Locate every uninfected red blood cell.
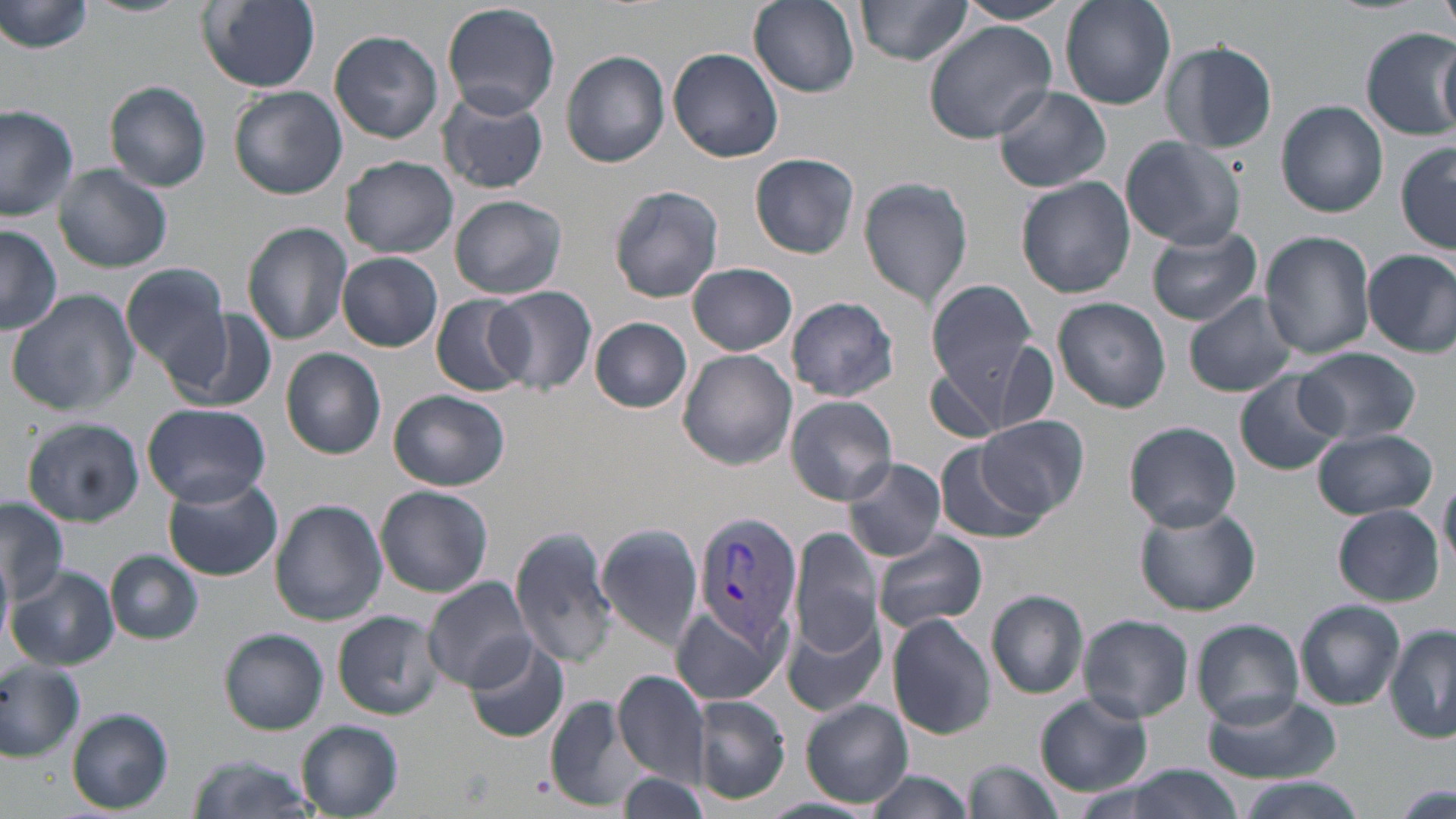
Approximate bounding boxes as [x1, y1, x2, y2] in pixels.
Uninfected red blood cells: [82, 0, 189, 18], [195, 0, 324, 93], [749, 0, 861, 98], [954, 0, 1073, 25], [1438, 0, 1456, 43], [2, 1, 95, 56], [855, 1, 972, 67], [1061, 1, 1176, 110], [442, 2, 561, 120], [923, 21, 1057, 144], [1360, 29, 1456, 139], [331, 31, 444, 143], [1160, 39, 1279, 155], [1437, 43, 1455, 133], [668, 48, 784, 164], [561, 50, 671, 168], [105, 81, 213, 192], [229, 85, 348, 201], [993, 85, 1111, 194], [437, 89, 549, 194], [1278, 101, 1388, 218], [0, 104, 79, 222], [1121, 136, 1246, 250], [1397, 143, 1455, 253], [750, 152, 860, 258], [341, 155, 458, 257], [54, 164, 172, 273], [859, 175, 975, 311], [1016, 177, 1136, 297], [608, 184, 726, 304], [450, 194, 567, 300], [242, 222, 354, 345], [0, 224, 61, 335], [1147, 226, 1262, 326], [1260, 230, 1377, 360], [1363, 248, 1456, 358], [337, 253, 444, 352], [688, 261, 798, 355], [121, 262, 232, 382], [925, 278, 1040, 405], [489, 286, 599, 393], [7, 289, 141, 416], [1184, 291, 1300, 398], [431, 294, 532, 396], [786, 296, 900, 401], [1053, 297, 1171, 413], [177, 310, 278, 413], [589, 317, 693, 413], [991, 342, 1057, 433], [1297, 347, 1420, 446], [280, 348, 387, 458], [678, 349, 796, 470], [925, 365, 1011, 443], [1234, 371, 1344, 477], [389, 389, 510, 491], [785, 395, 899, 506], [142, 402, 270, 507], [978, 417, 1087, 519], [24, 418, 145, 525], [1124, 421, 1241, 531], [1313, 429, 1438, 520], [932, 441, 1045, 547], [843, 457, 948, 563], [162, 475, 283, 582], [1439, 476, 1456, 577], [376, 485, 494, 598], [314, 489, 446, 609], [0, 497, 71, 603], [272, 498, 388, 627], [1134, 504, 1261, 615], [1333, 505, 1444, 605], [596, 523, 704, 648], [787, 524, 886, 669], [509, 529, 618, 666], [870, 531, 988, 635], [106, 550, 203, 645], [1, 556, 13, 649], [8, 565, 118, 671], [424, 576, 534, 691], [987, 589, 1088, 699], [1296, 599, 1405, 711], [671, 603, 788, 706], [334, 610, 444, 721], [784, 613, 886, 718], [887, 615, 995, 739], [1078, 615, 1193, 724], [1191, 619, 1305, 728], [1386, 626, 1455, 745], [220, 629, 328, 733], [463, 637, 572, 745], [0, 662, 86, 759], [612, 670, 710, 786], [1034, 691, 1153, 796], [1200, 694, 1344, 783], [543, 695, 651, 811], [693, 696, 791, 804], [802, 699, 913, 807], [68, 708, 172, 814], [297, 722, 405, 818], [186, 753, 317, 819], [966, 758, 1063, 819], [1077, 765, 1250, 819], [617, 772, 713, 817], [864, 772, 976, 819], [1236, 779, 1363, 819], [1387, 781, 1456, 819], [755, 796, 877, 819].

Summary:
  - Plasmodium vivax-infected red blood cell locations: [693, 511, 801, 649]
  - Slide-level diagnosis: Plasmodium vivax
  - Field of view: one of a larger specimen
  - Modality: light microscopy
  - Preparation: thin blood film
  - Magnification: 1000x
  - Image size: 1456×819 pixels
  - Stain: May-Grünwald-Giemsa